Classify this cell by malaria status.
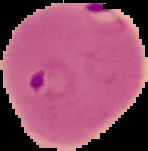

Parasitized.

Summary:
  - Image type: cell region segmented out of the field of view; surrounding area masked to black
  - Preparation: thin blood smear
  - Image size: 148×151 pixels